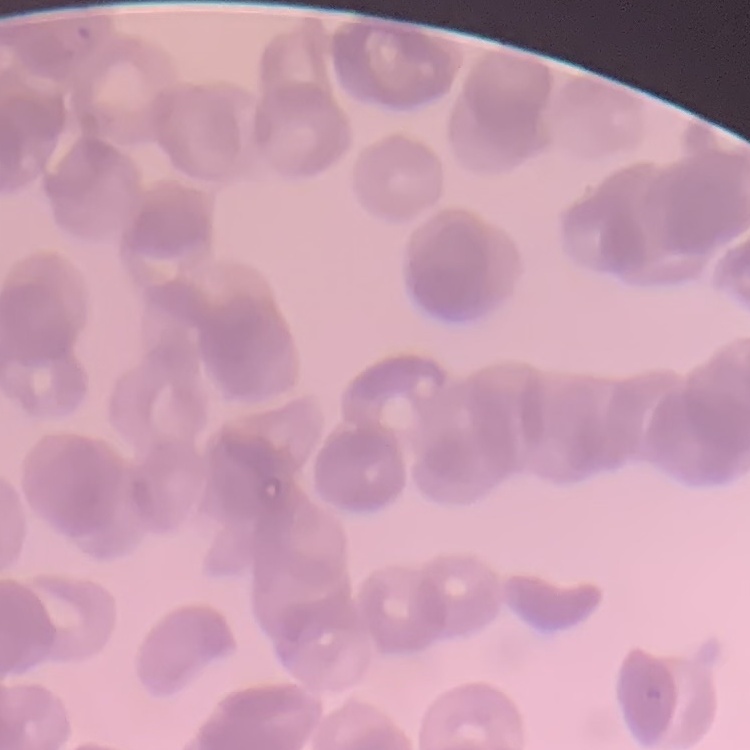

The red blood cells exhibit rouleaux formation. Field's or Giemsa stain. Square crop of a larger photomicrograph. Thin peripheral smear.